Name the blood parasite species.
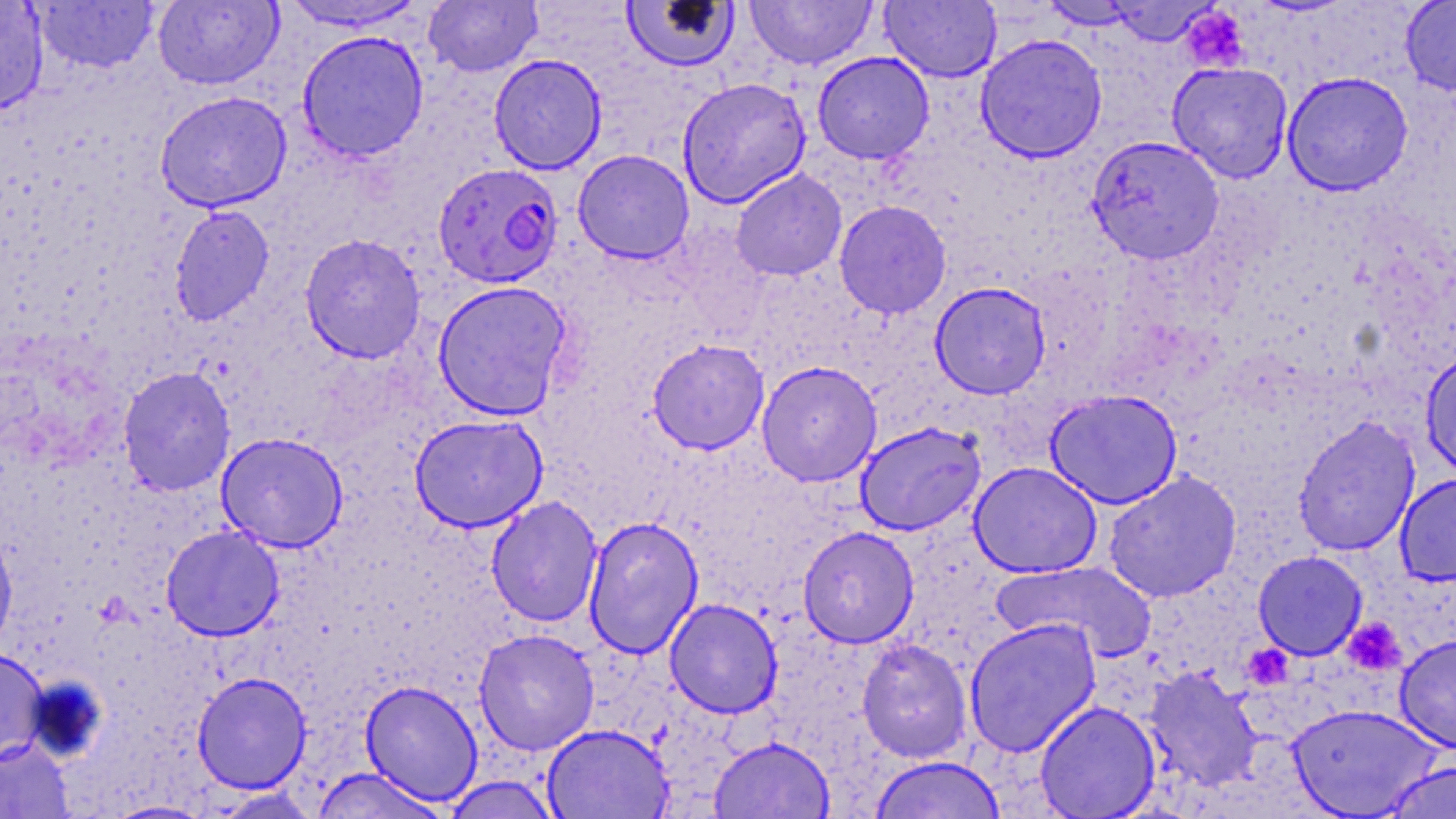

Plasmodium falciparum.

field of view = single
Plasmodium falciparum-infected red blood cell locations = approximate bounding boxes as named x1/y1/x2/y2 corners in pixels: (x1=433, y1=163, x2=564, y2=288)
magnification = 1000x
preparation = thin blood film
uninfected red blood cell locations = approximate bounding boxes as named x1/y1/x2/y2 corners in pixels: (x1=0, y1=0, x2=50, y2=116), (x1=276, y1=0, x2=432, y2=34), (x1=620, y1=0, x2=740, y2=73), (x1=743, y1=0, x2=879, y2=71), (x1=880, y1=0, x2=1002, y2=82), (x1=1399, y1=0, x2=1456, y2=96), (x1=32, y1=1, x2=160, y2=74), (x1=152, y1=1, x2=284, y2=91), (x1=423, y1=1, x2=543, y2=77), (x1=1038, y1=1, x2=1147, y2=30), (x1=1101, y1=1, x2=1220, y2=47), (x1=296, y1=30, x2=429, y2=162), (x1=974, y1=33, x2=1108, y2=163), (x1=812, y1=52, x2=934, y2=164), (x1=488, y1=53, x2=607, y2=175), (x1=1166, y1=62, x2=1293, y2=183), (x1=1282, y1=71, x2=1413, y2=196), (x1=677, y1=77, x2=811, y2=208), (x1=154, y1=90, x2=292, y2=213), (x1=1087, y1=135, x2=1224, y2=263), (x1=572, y1=149, x2=694, y2=264), (x1=730, y1=169, x2=847, y2=281), (x1=834, y1=200, x2=951, y2=319), (x1=168, y1=204, x2=275, y2=327), (x1=299, y1=234, x2=426, y2=364), (x1=432, y1=280, x2=573, y2=421), (x1=929, y1=281, x2=1051, y2=399), (x1=647, y1=339, x2=770, y2=454), (x1=1420, y1=350, x2=1456, y2=481), (x1=756, y1=360, x2=882, y2=487), (x1=117, y1=366, x2=235, y2=497), (x1=1044, y1=389, x2=1184, y2=509), (x1=409, y1=414, x2=548, y2=533), (x1=1292, y1=414, x2=1421, y2=556), (x1=854, y1=421, x2=986, y2=536), (x1=215, y1=432, x2=349, y2=552), (x1=969, y1=462, x2=1102, y2=578), (x1=1101, y1=470, x2=1243, y2=603), (x1=1394, y1=472, x2=1456, y2=586), (x1=485, y1=496, x2=603, y2=628), (x1=583, y1=516, x2=704, y2=658), (x1=0, y1=525, x2=18, y2=654), (x1=160, y1=525, x2=285, y2=641), (x1=797, y1=526, x2=919, y2=648), (x1=1252, y1=550, x2=1368, y2=661), (x1=992, y1=560, x2=1157, y2=662), (x1=664, y1=598, x2=783, y2=718), (x1=963, y1=617, x2=1102, y2=757), (x1=473, y1=629, x2=599, y2=755), (x1=1394, y1=632, x2=1456, y2=753), (x1=857, y1=638, x2=973, y2=763), (x1=0, y1=647, x2=50, y2=764), (x1=1142, y1=665, x2=1264, y2=793), (x1=192, y1=671, x2=312, y2=793), (x1=359, y1=680, x2=484, y2=805), (x1=1035, y1=701, x2=1160, y2=818), (x1=1287, y1=703, x2=1445, y2=818), (x1=542, y1=723, x2=673, y2=819), (x1=709, y1=736, x2=835, y2=819), (x1=0, y1=738, x2=74, y2=819), (x1=866, y1=755, x2=1010, y2=818), (x1=1379, y1=759, x2=1456, y2=819), (x1=310, y1=767, x2=450, y2=819), (x1=442, y1=776, x2=562, y2=818), (x1=209, y1=788, x2=323, y2=818), (x1=103, y1=800, x2=216, y2=818)
modality = optical microscopy
stain = May-Grünwald-Giemsa
platelet locations = approximate bounding boxes as named x1/y1/x2/y2 corners in pixels: (x1=1181, y1=6, x2=1250, y2=73), (x1=1342, y1=617, x2=1407, y2=675)
image size = 1456×819 pixels